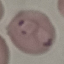 Malaria status: parasitized. Giemsa stain. Automatically extracted cell patch, resized to 64 × 64 pixels. Photographed with a smartphone camera at the microscope eyepiece. Thin blood film.